Describe the morphology of the red blood cells.
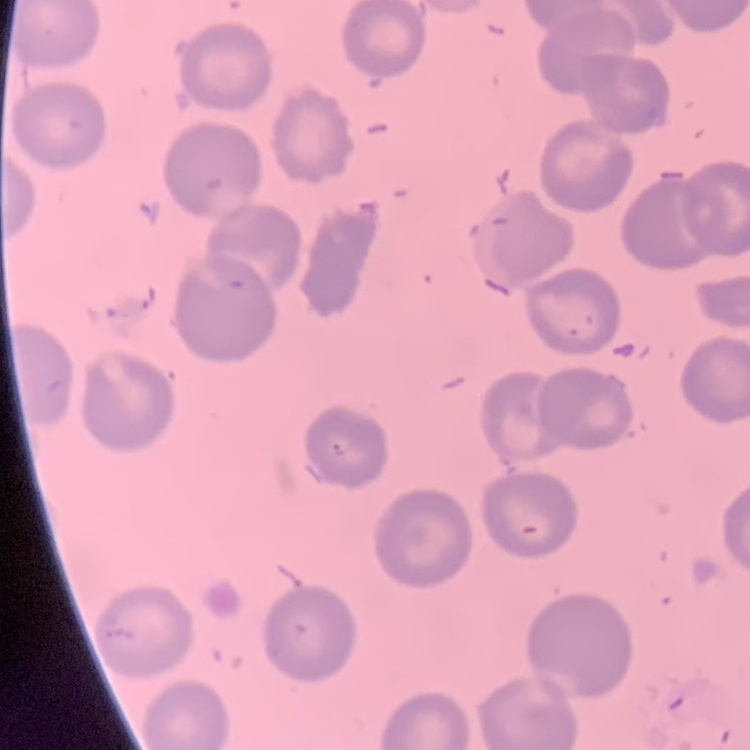
They show no rouleaux formation.

stain = Field's or Giemsa
preparation = thin blood film
image type = square crop of a larger photomicrograph